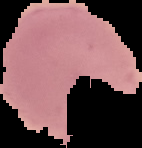
Malaria status: parasitized. From a thin blood smear. The area outside the segmented cell region is set to black. Image is 142×148 pixels.